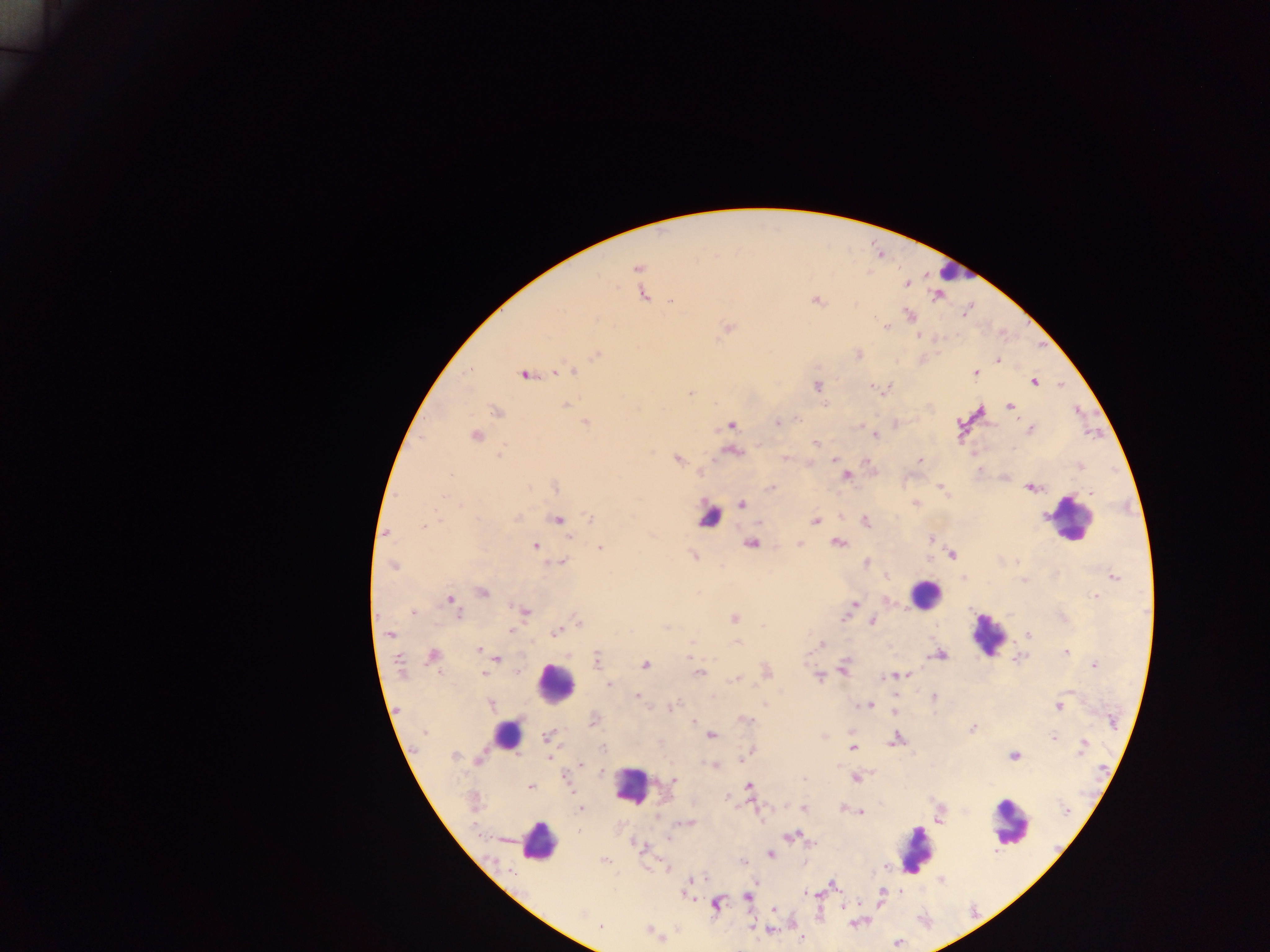
Approximate centers as [x, y] in pixels. Plasmodium parasite locations: [637, 268], [907, 284], [643, 294], [937, 296], [670, 301], [816, 301], [910, 315], [598, 318], [729, 327], [885, 327], [919, 336], [596, 355], [859, 355], [997, 360], [558, 371], [569, 371], [975, 373], [524, 374], [1034, 382], [817, 386], [872, 387], [691, 393], [565, 404], [825, 405], [1010, 406], [496, 412], [777, 422], [586, 423], [731, 425], [1030, 429], [875, 435], [476, 436], [815, 443], [1014, 449], [732, 451], [500, 453], [785, 458], [678, 460], [834, 460], [920, 460], [867, 461], [979, 469], [450, 475], [846, 476], [555, 487], [940, 487], [529, 488], [1030, 488], [770, 489], [1091, 494], [443, 497], [742, 504], [916, 504], [517, 518], [590, 518], [558, 519], [815, 521], [866, 522], [423, 525], [387, 532], [568, 537], [930, 540], [750, 543], [838, 543], [799, 544], [535, 546], [600, 547], [952, 555], [694, 556], [558, 563], [866, 563], [393, 566], [1114, 576], [963, 578], [1024, 580], [482, 592], [1095, 596], [450, 599], [854, 604], [413, 612], [525, 612], [457, 614], [734, 619], [843, 619], [579, 622], [872, 622], [666, 627], [512, 630], [390, 633], [555, 633], [1029, 635], [692, 642], [737, 642], [821, 644], [479, 651], [1066, 652], [433, 655], [940, 655], [597, 658], [1017, 658], [496, 659], [399, 663], [645, 665], [1094, 665], [844, 667], [519, 672], [767, 672], [484, 673], [698, 673], [904, 675], [897, 676], [819, 677], [891, 677], [735, 679], [609, 684], [1070, 691], [637, 696], [934, 697], [895, 699], [491, 704], [765, 705], [868, 705], [672, 706], [1059, 707], [894, 710], [593, 720], [746, 720], [694, 721], [1112, 721], [972, 729], [424, 732], [712, 735], [824, 736], [1054, 737], [547, 738], [896, 739], [1083, 746], [603, 748], [853, 748], [750, 751], [454, 756], [745, 756], [1014, 756], [743, 759], [479, 761], [581, 765], [714, 765], [601, 770], [567, 778], [855, 778], [803, 779], [674, 780], [749, 786], [530, 787], [581, 809], [804, 809], [1067, 810], [861, 813], [687, 823], [793, 836], [668, 838], [813, 843], [641, 847], [771, 854], [605, 860], [741, 860], [885, 867], [942, 880], [688, 884], [833, 885], [806, 893], [882, 893], [686, 894], [747, 897], [715, 904], [844, 906], [774, 909], [580, 913], [601, 927], [770, 930], [801, 939], [898, 943]. Leukocyte locations: [952, 272], [709, 517], [1071, 520], [924, 594], [988, 634], [555, 683], [505, 733], [632, 786], [1010, 822], [538, 842], [917, 851]. Image is 1270×952 pixels. Single field of view. Collected in Ghana. Photographed through a microscope with a mobile-phone camera. Thick blood smear.